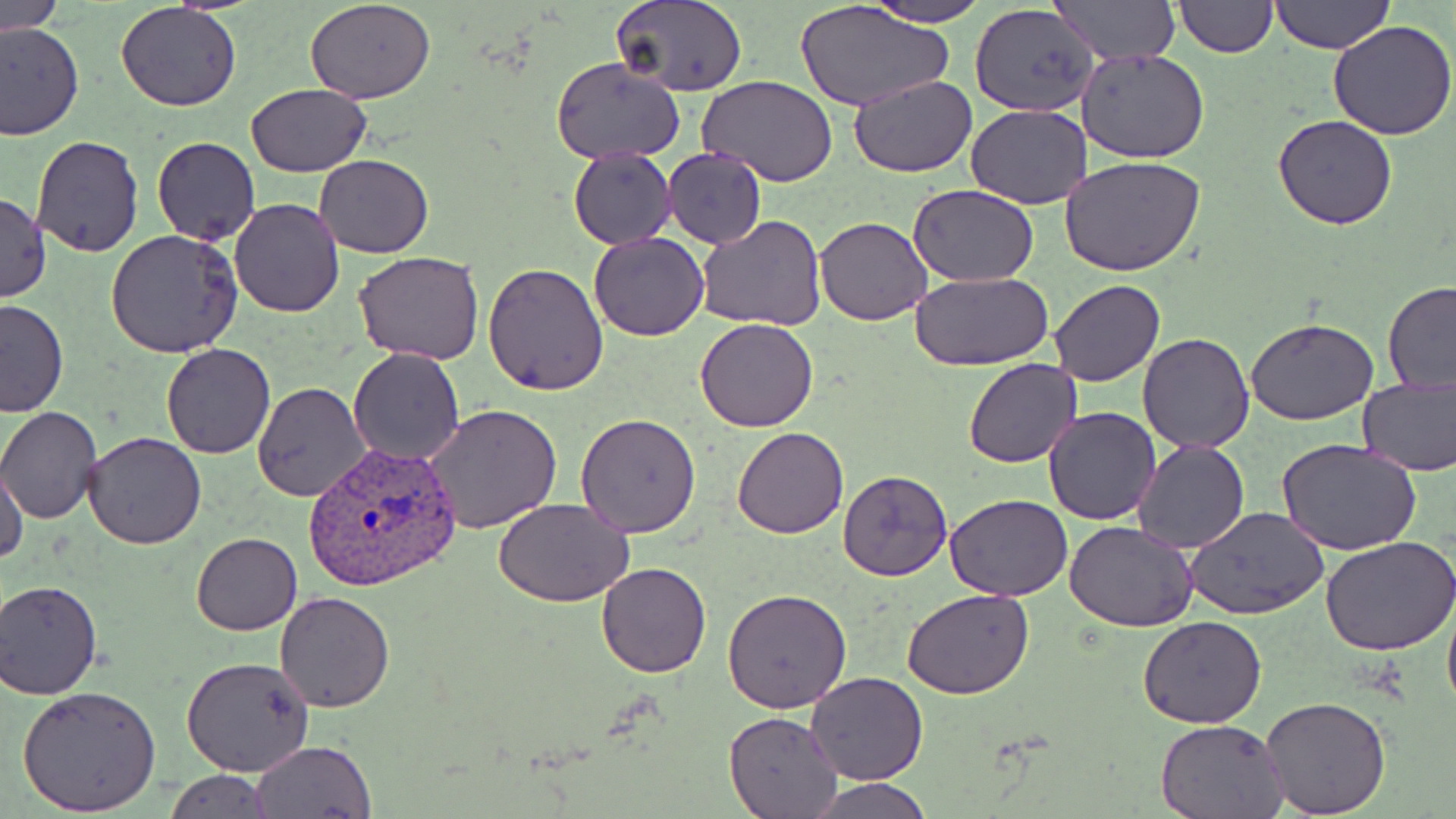

Summary:
  - Coordinate format: approximate bounding boxes as [x1, y1, x2, y2] in pixels
  - Uninfected red blood cell locations: [305, 0, 436, 103], [610, 0, 750, 96], [864, 0, 988, 26], [1050, 0, 1181, 66], [1271, 0, 1393, 54], [1, 1, 67, 33], [792, 1, 954, 112], [1174, 1, 1276, 57], [970, 3, 1100, 118], [115, 4, 242, 112], [1328, 19, 1456, 139], [0, 21, 82, 141], [1076, 47, 1208, 165], [551, 57, 685, 166], [848, 74, 977, 177], [700, 76, 840, 187], [246, 84, 370, 177], [967, 104, 1091, 209], [1273, 113, 1397, 231], [29, 136, 146, 258], [151, 137, 260, 245], [568, 146, 676, 249], [578, 146, 689, 342], [662, 147, 767, 247], [314, 154, 433, 257], [1061, 156, 1206, 278], [907, 183, 1039, 285], [0, 193, 50, 302], [229, 197, 343, 317], [814, 215, 933, 326], [694, 216, 826, 331], [104, 230, 244, 358], [589, 234, 709, 341], [356, 251, 485, 365], [483, 263, 610, 396], [908, 272, 1053, 371], [1046, 279, 1166, 386], [1381, 282, 1456, 395], [0, 300, 68, 417], [696, 318, 818, 433], [1246, 318, 1377, 425], [1136, 333, 1255, 454], [162, 343, 275, 459], [349, 346, 465, 465], [963, 358, 1081, 468], [1357, 375, 1456, 475], [252, 382, 371, 502], [424, 404, 563, 536], [0, 407, 102, 523], [1043, 407, 1161, 525], [576, 413, 703, 537], [733, 426, 848, 539], [81, 432, 206, 548], [1133, 439, 1250, 553], [1278, 440, 1424, 555], [0, 466, 29, 568], [838, 469, 954, 582], [944, 492, 1072, 602], [493, 498, 634, 606], [1188, 507, 1330, 618], [1064, 520, 1198, 632], [192, 532, 302, 634], [1321, 537, 1456, 657], [596, 562, 711, 678], [0, 580, 103, 697], [903, 586, 1034, 699], [722, 589, 852, 712], [1442, 589, 1456, 723], [275, 591, 394, 712], [1138, 615, 1268, 729], [181, 654, 315, 776], [806, 671, 928, 785], [17, 686, 162, 816], [1261, 695, 1392, 815], [724, 712, 844, 818], [1155, 717, 1289, 818], [253, 740, 376, 818], [163, 770, 275, 817], [806, 777, 932, 817]
  - Plasmodium vivax-infected red blood cell locations: [305, 439, 464, 591]
  - Slide-level diagnosis: Plasmodium vivax
  - Preparation: thin blood film
  - Field of view: one of a larger specimen
  - Modality: optical microscopy
  - Magnification: 1000x
  - Image size: 1456×819 pixels
  - Stain: May-Grünwald-Giemsa